Assess this cell for malaria.
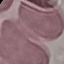
Uninfected.

{
  "stain": "Giemsa",
  "preparation": "thin blood film",
  "capture": "smartphone through the microscope eyepiece",
  "image_type": "automatically extracted cell patch, resized to 64 × 64 pixels"
}